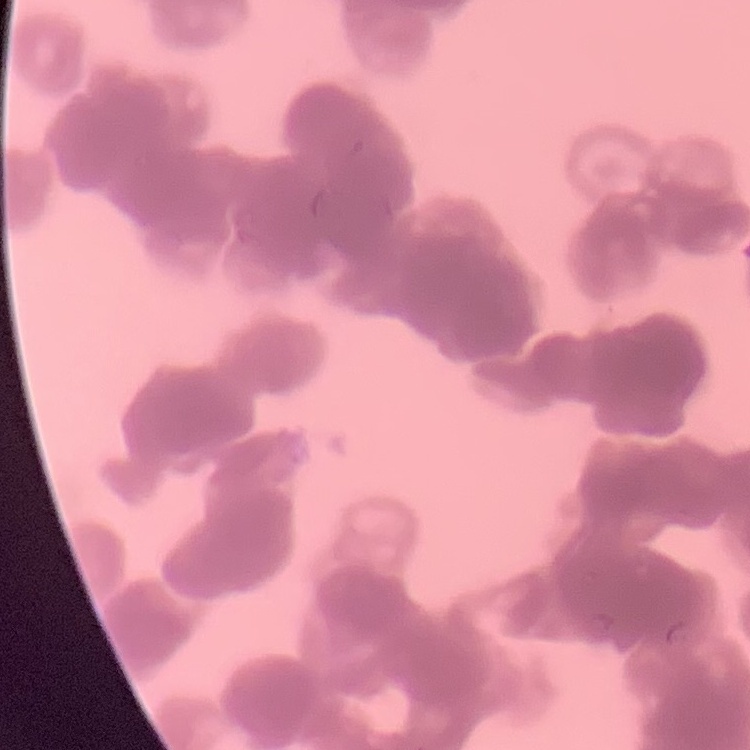

Summary:
  - Erythrocyte morphology: rouleaux formation
  - Image type: square crop of a larger photomicrograph
  - Preparation: thin peripheral smear
  - Stain: Field's or Giemsa